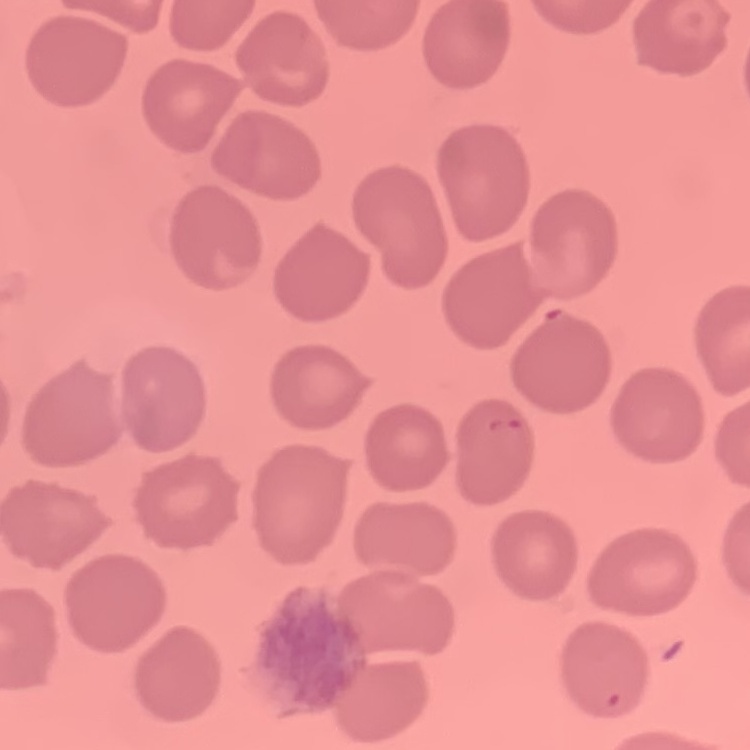

The red blood cells exhibit no rouleaux formation. Square crop of a larger photomicrograph. Thin peripheral smear. Stained with either Field's or Giemsa.